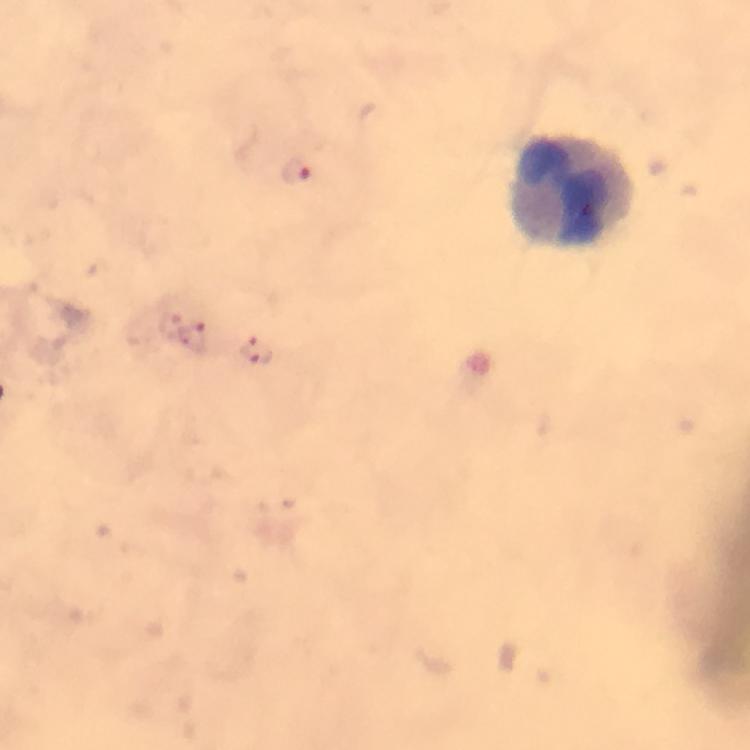
magnification = 100x
image size = 750×750 pixels
immersion oil = applied
capture = smartphone photograph through a microscope
cropped from = one field of view
leukocyte locations = approximate centers as (x, y) in pixels: (572, 189)
stain = Giemsa
Plasmodium parasite locations = approximate centers as (x, y) in pixels: (298, 173), (172, 324), (197, 339), (257, 351)
context = from a malaria diagnostic workup
preparation = thick blood smear